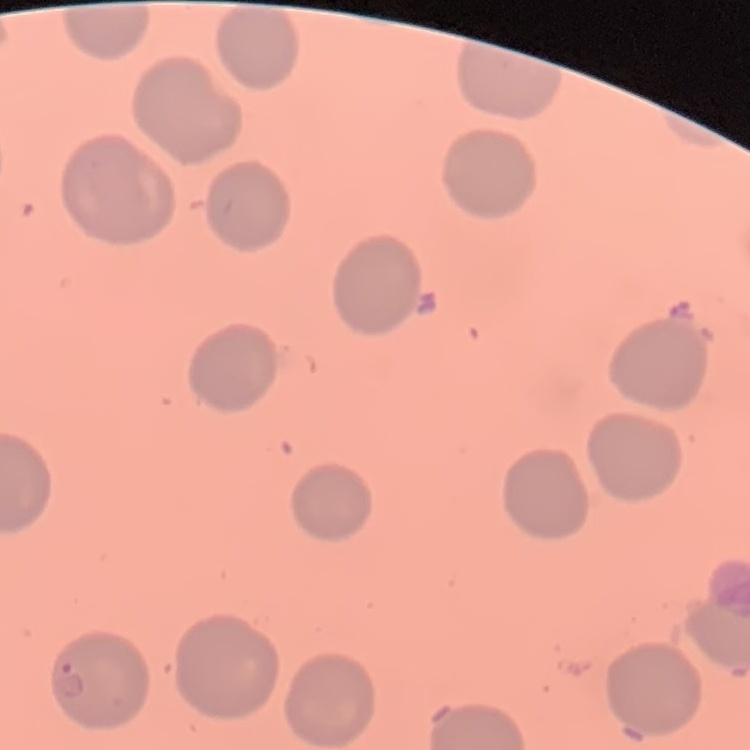
red blood cell morphology = no rouleaux formation
preparation = thin blood film
stain = Field's or Giemsa
image type = one tile cut from a larger photomicrograph